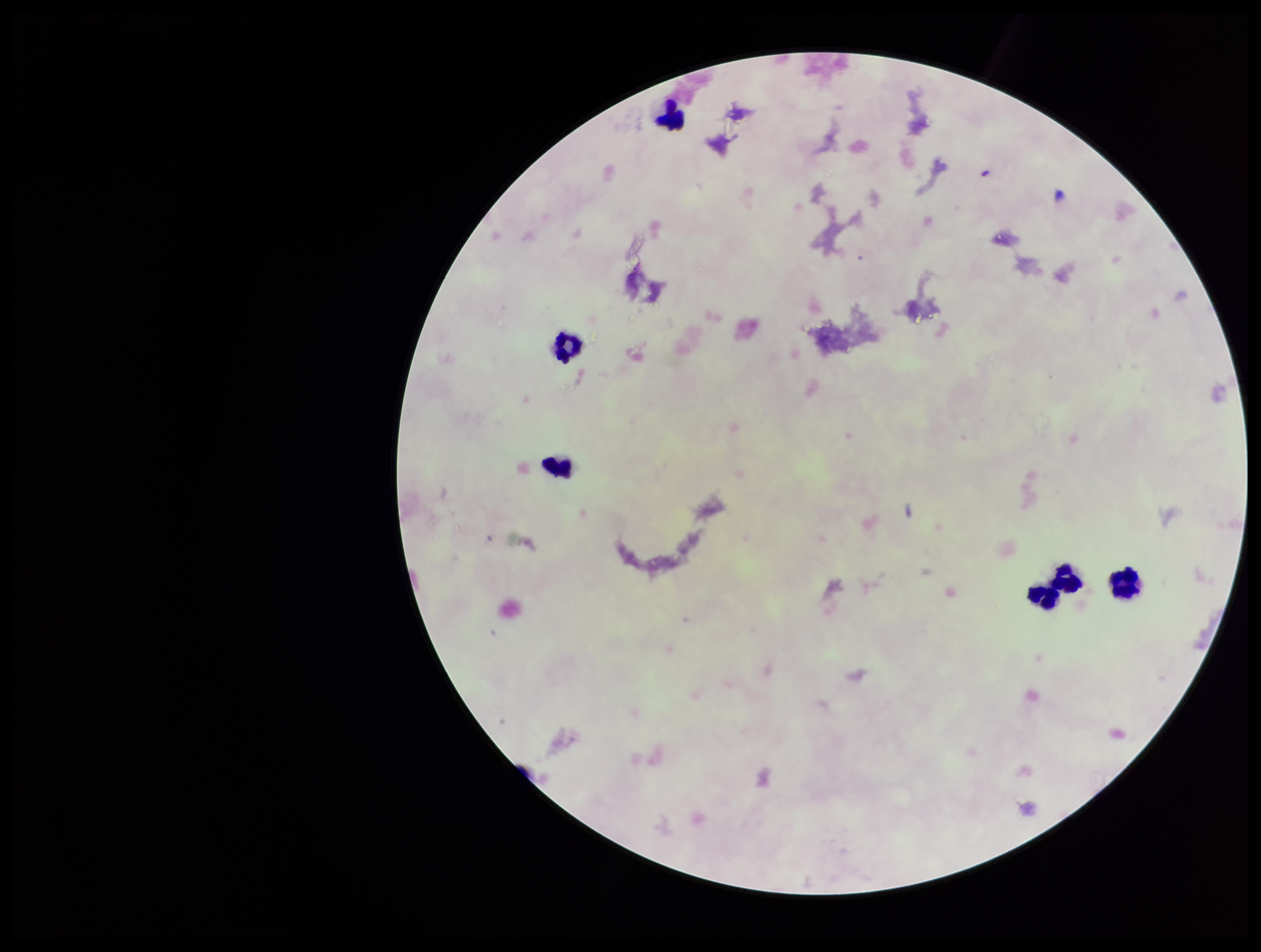
Parasite count: 0. Single field of view. Image is 1261×952 pixels. Plasmodium parasites: none seen. Preparation: thick smear. Leukocyte count: 5. Patient malaria status: negative. Photographed through the microscope eyepiece with a smartphone camera. Giemsa stain.